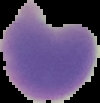 Image is 100×103 pixels. Malaria status: uninfected. The area outside the segmented cell region is set to black. From a thin blood smear.